Report the malaria status of this cell.
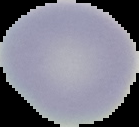
Uninfected.

image type = segmented cell region with the area outside set to black
preparation = thin blood smear
image size = 139×127 pixels